Locate every Plasmodium parasite.
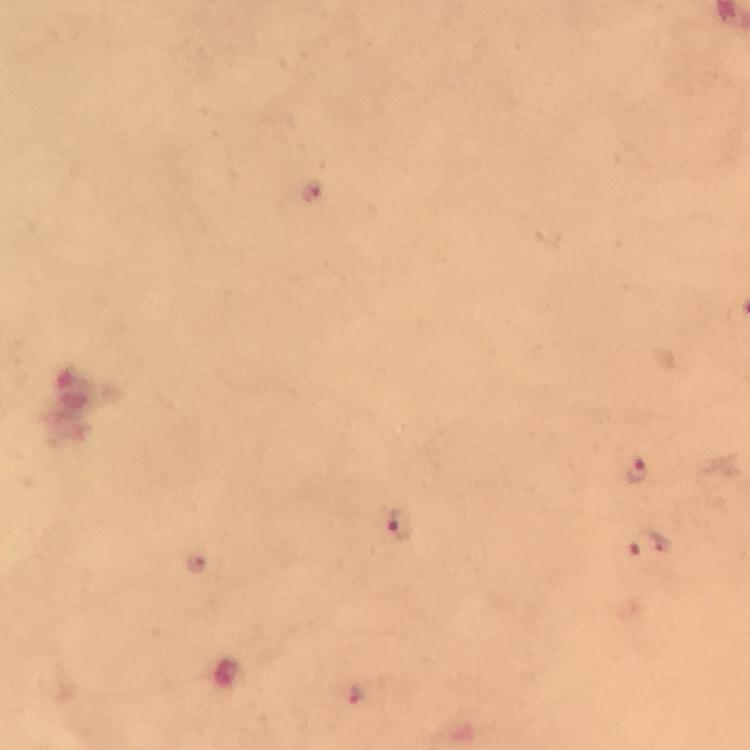
Approximate centers as {x, y} in pixels.
Plasmodium parasites: {312, 192}, {636, 470}, {402, 525}, {648, 546}, {196, 561}, {356, 693}.

From a diagnostic examination for malaria. Cropped region of a single field of view. Image is 750×750 pixels. Immersion oil applied. At 100x magnification. Smartphone photograph taken through a microscope. Thick smear. Giemsa stain.